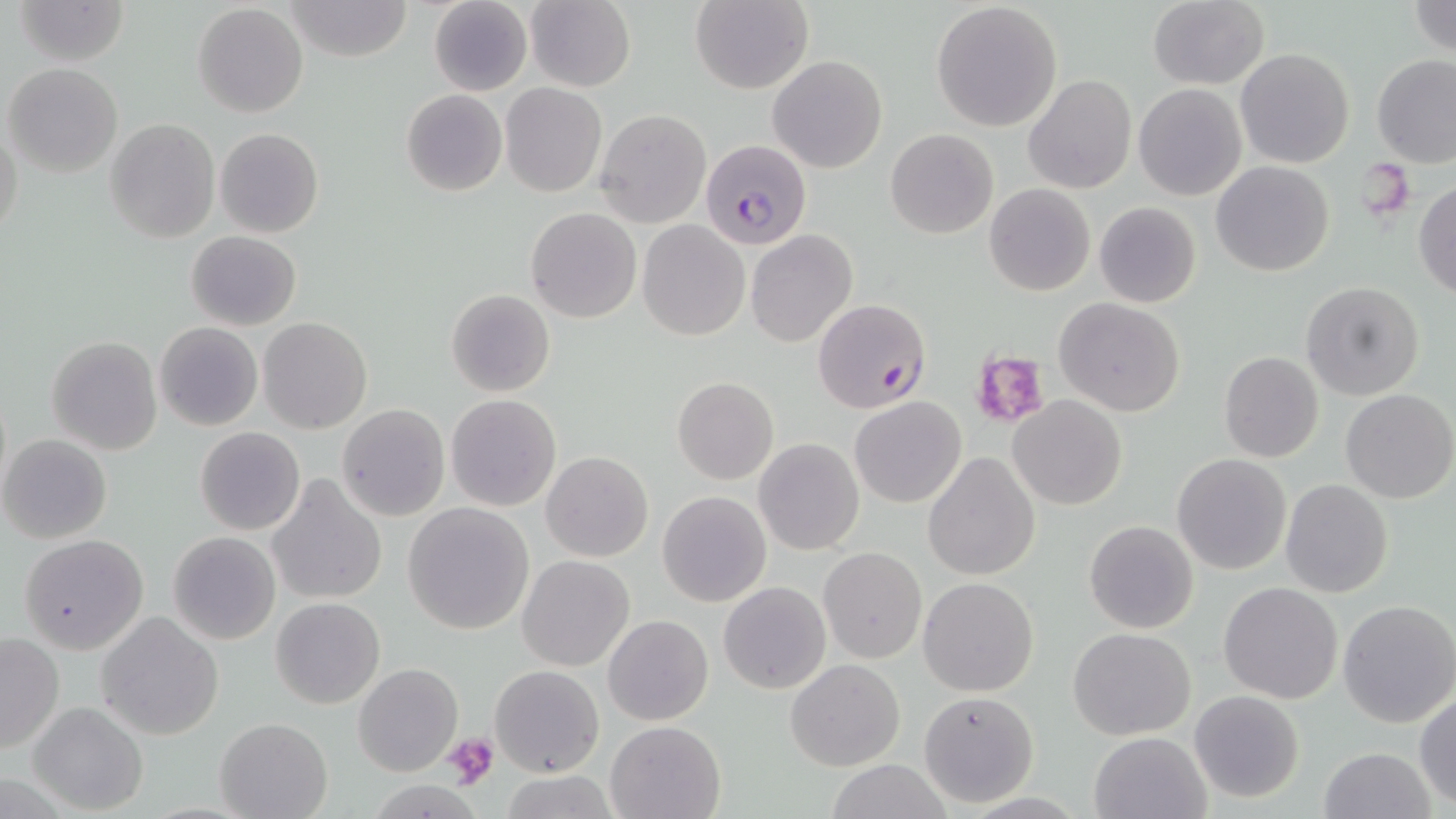
slide-level diagnosis = Plasmodium falciparum
stain = May-Grünwald-Giemsa
Plasmodium falciparum-infected red blood cell locations = approximate bounding boxes as named x1/y1/x2/y2 corners in pixels: (x1=699, y1=139, x2=812, y2=249), (x1=813, y1=298, x2=929, y2=413)
platelet locations = approximate bounding boxes as named x1/y1/x2/y2 corners in pixels: (x1=967, y1=346, x2=1051, y2=432), (x1=443, y1=732, x2=499, y2=788)
preparation = thin blood film
modality = optical microscopy
magnification = 1000x
uninfected red blood cell locations = approximate bounding boxes as named x1/y1/x2/y2 corners in pixels: (x1=13, y1=0, x2=130, y2=66), (x1=286, y1=0, x2=412, y2=62), (x1=428, y1=0, x2=533, y2=96), (x1=525, y1=0, x2=636, y2=91), (x1=1147, y1=0, x2=1269, y2=88), (x1=1408, y1=0, x2=1456, y2=58), (x1=688, y1=1, x2=813, y2=93), (x1=931, y1=2, x2=1063, y2=132), (x1=193, y1=3, x2=308, y2=117), (x1=1235, y1=47, x2=1356, y2=169), (x1=1372, y1=53, x2=1456, y2=166), (x1=769, y1=55, x2=888, y2=173), (x1=5, y1=63, x2=123, y2=178), (x1=1024, y1=75, x2=1137, y2=193), (x1=500, y1=84, x2=607, y2=197), (x1=1135, y1=84, x2=1247, y2=200), (x1=400, y1=88, x2=508, y2=196), (x1=496, y1=94, x2=702, y2=209), (x1=594, y1=108, x2=711, y2=227), (x1=105, y1=118, x2=219, y2=243), (x1=0, y1=123, x2=23, y2=241), (x1=215, y1=128, x2=324, y2=238), (x1=885, y1=128, x2=998, y2=239), (x1=1212, y1=161, x2=1333, y2=277), (x1=1413, y1=180, x2=1456, y2=298), (x1=985, y1=184, x2=1096, y2=297), (x1=1094, y1=201, x2=1202, y2=308), (x1=526, y1=207, x2=642, y2=322), (x1=637, y1=220, x2=750, y2=340), (x1=746, y1=230, x2=858, y2=348), (x1=186, y1=231, x2=301, y2=330), (x1=1301, y1=281, x2=1425, y2=401), (x1=446, y1=289, x2=556, y2=396), (x1=1053, y1=298, x2=1186, y2=418), (x1=259, y1=318, x2=372, y2=435), (x1=154, y1=323, x2=263, y2=432), (x1=46, y1=336, x2=162, y2=456), (x1=1219, y1=351, x2=1324, y2=462), (x1=672, y1=377, x2=778, y2=484), (x1=1340, y1=388, x2=1455, y2=503), (x1=446, y1=394, x2=561, y2=511), (x1=850, y1=395, x2=966, y2=508), (x1=1010, y1=395, x2=1127, y2=510), (x1=337, y1=404, x2=450, y2=520), (x1=888, y1=405, x2=1010, y2=534), (x1=196, y1=427, x2=305, y2=535), (x1=2, y1=434, x2=112, y2=544), (x1=754, y1=438, x2=864, y2=555), (x1=541, y1=450, x2=653, y2=562), (x1=923, y1=451, x2=1041, y2=581), (x1=1172, y1=453, x2=1291, y2=575), (x1=266, y1=475, x2=388, y2=606), (x1=1281, y1=480, x2=1394, y2=599), (x1=658, y1=491, x2=772, y2=607), (x1=403, y1=502, x2=534, y2=634), (x1=200, y1=514, x2=341, y2=644), (x1=1084, y1=520, x2=1199, y2=634), (x1=168, y1=532, x2=281, y2=645), (x1=18, y1=534, x2=149, y2=654), (x1=818, y1=546, x2=927, y2=663), (x1=518, y1=555, x2=635, y2=672), (x1=918, y1=576, x2=1038, y2=696), (x1=718, y1=581, x2=831, y2=693), (x1=1219, y1=583, x2=1343, y2=702), (x1=271, y1=596, x2=385, y2=709), (x1=1338, y1=600, x2=1455, y2=727), (x1=96, y1=611, x2=224, y2=740), (x1=604, y1=614, x2=714, y2=726), (x1=1069, y1=628, x2=1195, y2=739), (x1=0, y1=629, x2=64, y2=757), (x1=785, y1=659, x2=905, y2=770), (x1=353, y1=664, x2=462, y2=776), (x1=490, y1=665, x2=604, y2=777), (x1=917, y1=690, x2=1040, y2=807), (x1=1415, y1=690, x2=1456, y2=810), (x1=1190, y1=691, x2=1303, y2=802), (x1=30, y1=701, x2=149, y2=816), (x1=215, y1=717, x2=333, y2=819), (x1=604, y1=719, x2=728, y2=819), (x1=1089, y1=731, x2=1209, y2=818), (x1=1320, y1=745, x2=1435, y2=819), (x1=825, y1=758, x2=952, y2=819), (x1=496, y1=771, x2=624, y2=819)
field of view = single
image size = 1456×819 pixels